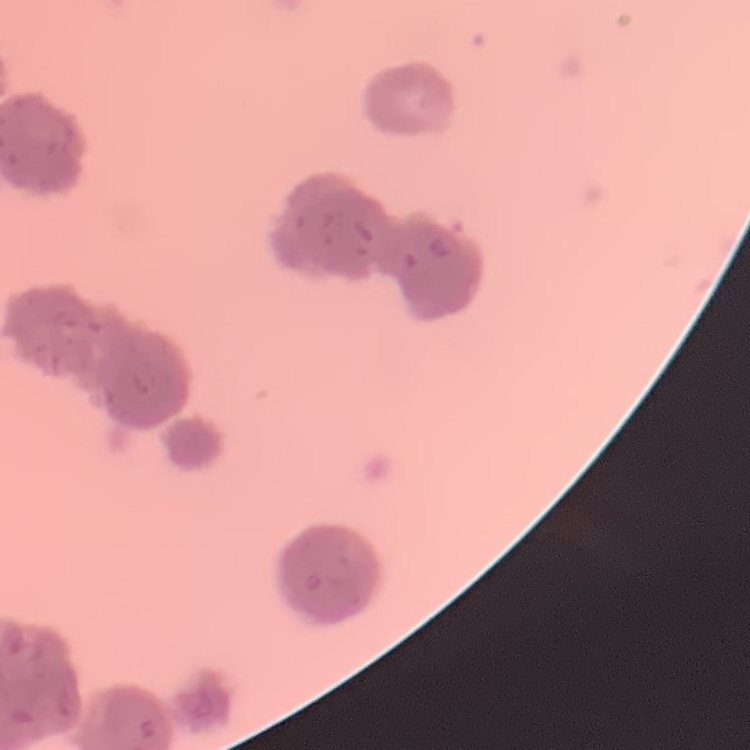
The red blood cells exhibit rouleaux formation. Thin blood film. One tile cut from a larger photomicrograph. Stained with either Field's or Giemsa.